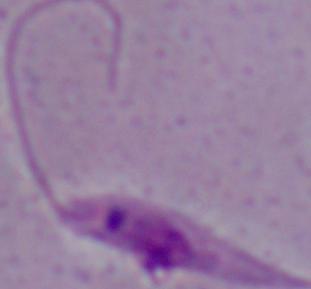

modality: photomicrograph
identification: Leishmania
magnification: 1000x